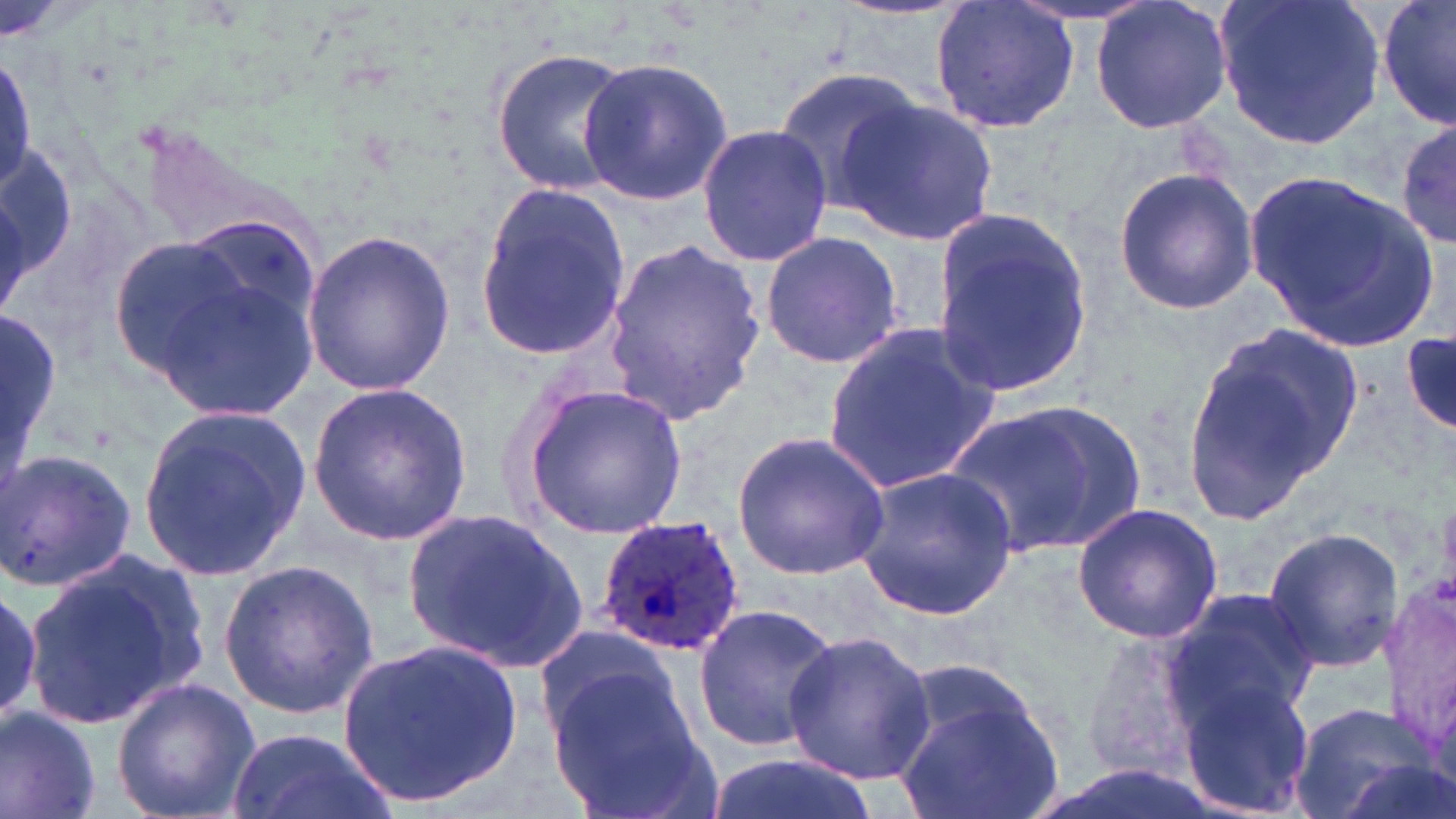

Summary:
  - Coordinate format: approximate bounding boxes as (x1, y1, x2, y2) in pixels
  - Plasmodium ovale-infected red blood cell locations: (593, 515, 745, 655)
  - Uninfected red blood cell locations: (931, 0, 1081, 137), (1090, 0, 1234, 136), (1215, 0, 1387, 148), (1378, 0, 1455, 132), (489, 47, 633, 196), (0, 53, 35, 195), (577, 55, 734, 208), (775, 66, 927, 216), (838, 95, 998, 248), (1393, 120, 1455, 248), (698, 124, 834, 266), (1113, 167, 1258, 315), (1243, 168, 1440, 353), (472, 177, 633, 364), (930, 212, 1094, 400), (300, 228, 455, 397), (759, 230, 906, 371), (105, 236, 258, 383), (603, 236, 769, 427), (136, 239, 327, 420), (1182, 318, 1364, 522), (822, 321, 1002, 498), (1400, 329, 1455, 437), (306, 382, 473, 544), (519, 384, 689, 539), (944, 399, 1150, 556), (139, 402, 310, 584), (732, 431, 891, 579), (0, 448, 136, 592), (853, 464, 1020, 621), (1070, 502, 1223, 644), (404, 507, 590, 679), (1262, 526, 1404, 673), (23, 550, 209, 730), (217, 556, 380, 719), (0, 578, 48, 728), (1164, 584, 1319, 735), (693, 604, 841, 753), (531, 625, 691, 759), (1075, 628, 1208, 786), (782, 630, 936, 786), (337, 637, 524, 810), (546, 669, 713, 819), (1176, 673, 1314, 818), (111, 675, 261, 819), (893, 681, 1064, 819), (1287, 702, 1440, 819), (0, 707, 100, 819), (227, 726, 389, 819), (706, 750, 872, 819)
  - Slide-level diagnosis: Plasmodium ovale
  - Stain: May-Grünwald-Giemsa
  - Field of view: single
  - Magnification: 1000x
  - Image size: 1456×819 pixels
  - Preparation: thin blood smear
  - Modality: optical microscopy